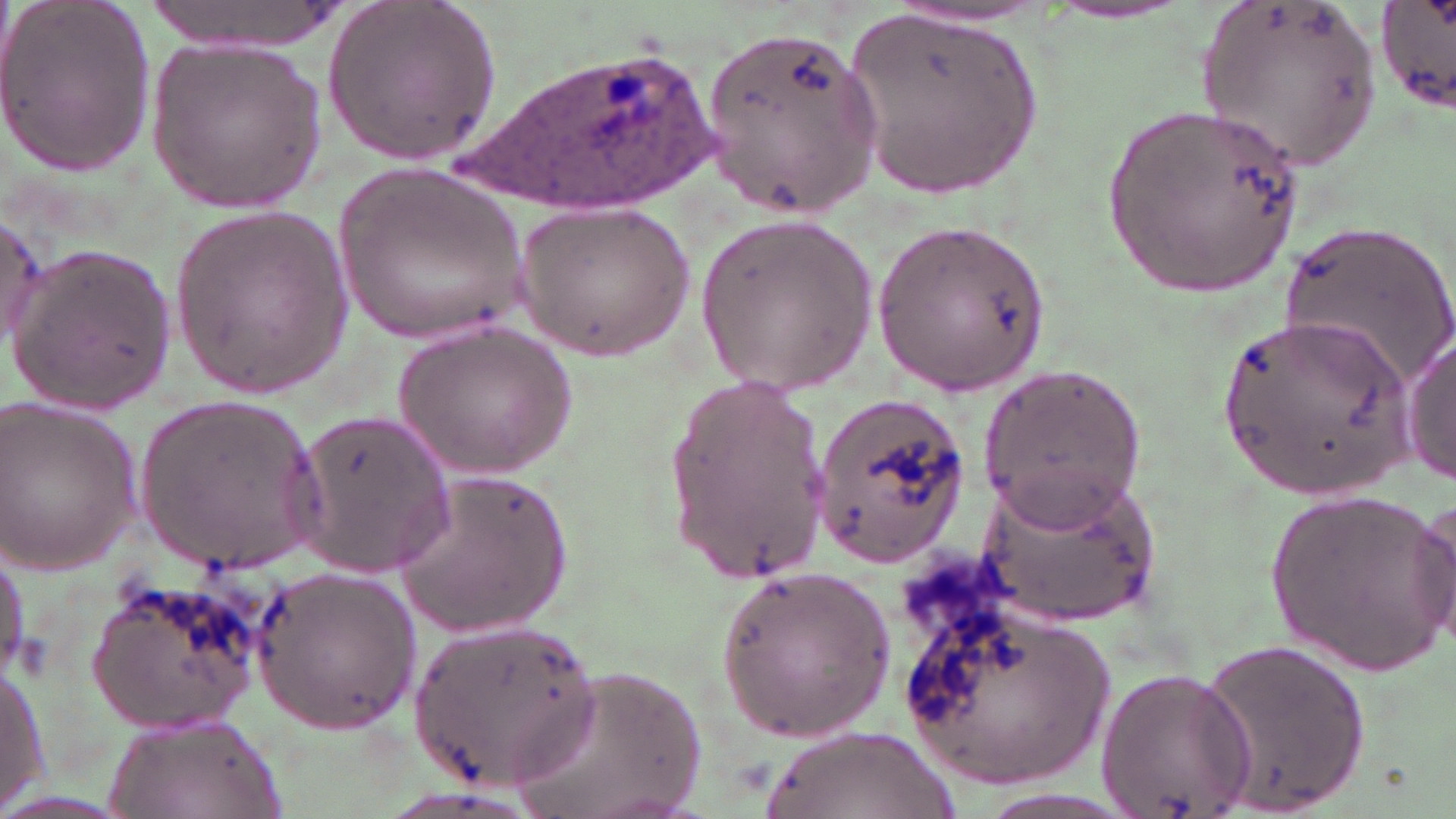
{
  "slide_level_diagnosis": "Plasmodium ovale",
  "uninfected_red_blood_cell_locations": "approximate bounding boxes as (x1,y1)-(x2,y2) corner pairs in pixels: (0,0)-(157,178), (133,0)-(357,56), (323,0)-(501,164), (1196,1)-(1382,176), (1376,1)-(1454,117), (844,4)-(1046,203), (1041,5)-(1196,26), (700,31)-(885,212), (145,38)-(328,213), (1097,101)-(1309,298), (332,163)-(532,347), (516,202)-(696,358), (170,203)-(353,399), (0,208)-(49,350), (696,214)-(877,396), (873,215)-(1052,395), (1276,223)-(1454,391), (11,245)-(178,413), (1215,313)-(1415,497), (395,318)-(580,480), (1400,335)-(1456,485), (979,362)-(1148,524), (659,372)-(835,580), (134,392)-(326,571), (813,392)-(969,569), (0,401)-(143,570), (295,408)-(454,575), (976,463)-(1161,625), (392,468)-(573,639), (1261,490)-(1456,673), (1411,493)-(1455,648), (0,543)-(28,679), (251,565)-(421,732), (716,566)-(901,740), (89,571)-(267,733), (897,583)-(1123,793), (408,618)-(603,790), (1197,632)-(1374,816), (0,658)-(49,811), (514,662)-(705,819), (1096,666)-(1256,814), (100,709)-(290,819), (761,726)-(959,819)",
  "field_of_view": "one of a larger specimen",
  "preparation": "thin blood film",
  "plasmodium_ovale_infected_red_blood_cell_locations": "approximate bounding boxes as (x1,y1)-(x2,y2) corner pairs in pixels: (461,42)-(720,218)",
  "stain": "May-Grünwald-Giemsa",
  "modality": "light microscopy",
  "image_size": "1456×819 pixels",
  "magnification": "1000x"
}